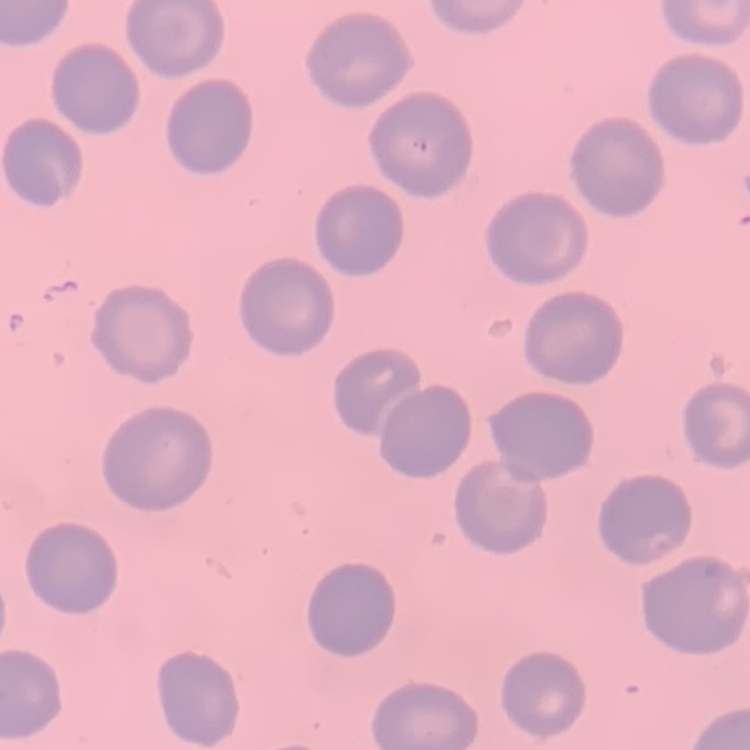
The erythrocytes show no rouleaux formation. Stained with either Field's or Giemsa. Square crop of a larger photomicrograph. Thin blood film.